Locate and identify every blood parasite.
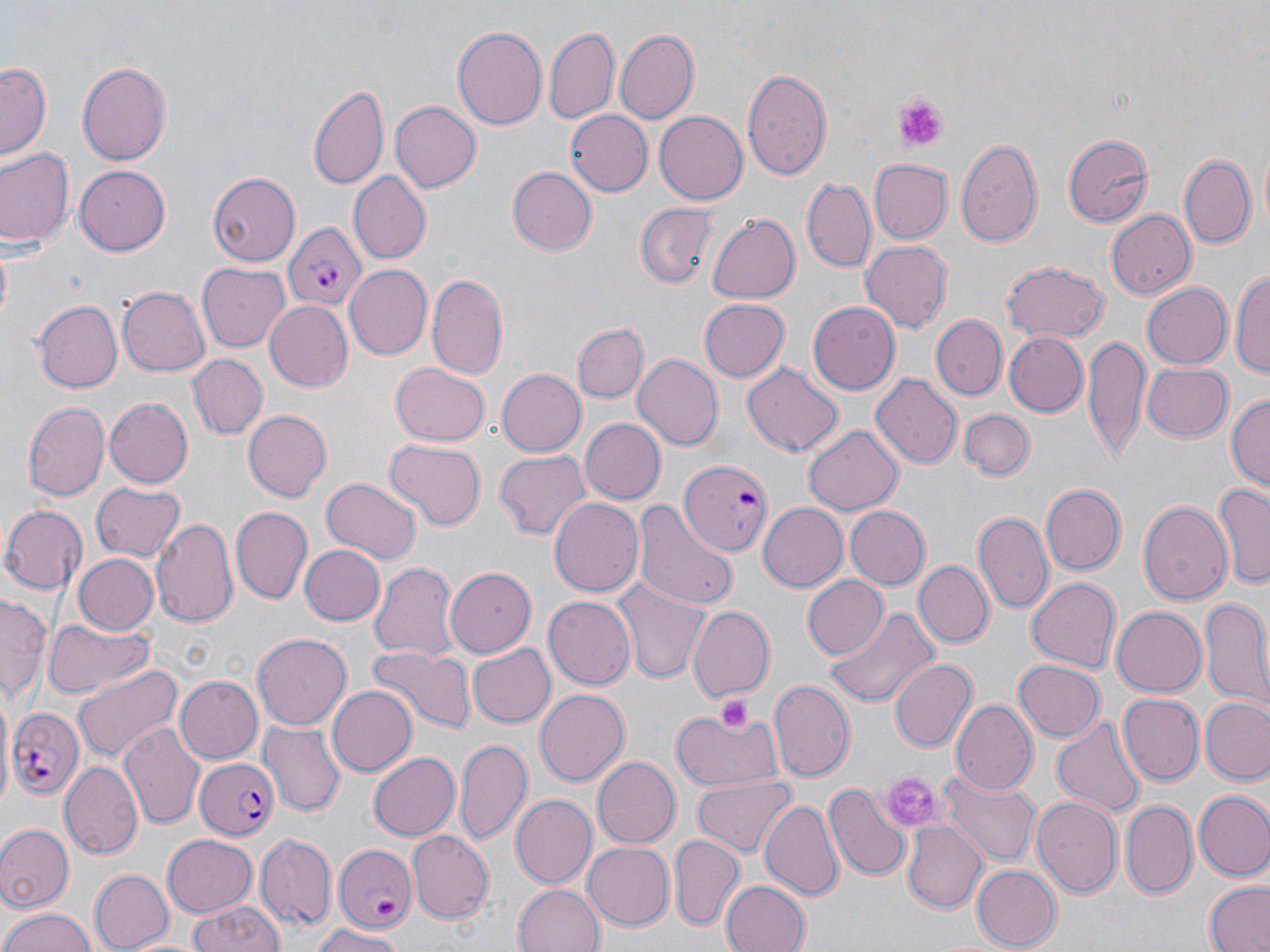
Approximate bounding boxes as (x1, y1, x2, y2) in pixels.
Plasmodium falciparum-infected red blood cells: (281, 220, 368, 311), (675, 456, 772, 559), (4, 707, 84, 799), (194, 758, 278, 841), (331, 843, 417, 934).
No Plasmodium ovale, Plasmodium malariae, Plasmodium vivax, Babesia divergens, or Trypanosoma brucei observed.

Uninfected red blood cell locations: (452, 23, 548, 132), (545, 25, 619, 125), (615, 29, 699, 125), (0, 60, 52, 160), (76, 60, 173, 166), (741, 68, 832, 183), (308, 80, 390, 190), (390, 100, 481, 193), (564, 110, 653, 197), (653, 110, 748, 205), (1064, 131, 1153, 226), (957, 138, 1042, 249), (0, 147, 77, 251), (1179, 151, 1255, 250), (868, 159, 952, 244), (73, 165, 171, 256), (507, 167, 596, 256), (207, 171, 300, 267), (347, 172, 431, 264), (803, 178, 876, 273), (637, 202, 718, 289), (1105, 209, 1194, 300), (708, 215, 800, 302), (859, 242, 952, 331), (998, 261, 1110, 342), (197, 262, 291, 353), (343, 264, 432, 362), (1233, 267, 1270, 382), (427, 273, 510, 383), (1140, 282, 1230, 370), (117, 286, 211, 378), (263, 298, 353, 390), (696, 298, 788, 383), (34, 301, 123, 392), (805, 301, 900, 395), (932, 315, 1007, 399), (572, 322, 647, 401), (1001, 331, 1087, 418), (1082, 336, 1148, 464), (188, 353, 267, 438), (631, 354, 722, 452), (739, 361, 843, 459), (1140, 362, 1231, 441), (389, 363, 489, 446), (496, 367, 586, 458), (871, 374, 961, 470), (1227, 394, 1270, 493), (104, 398, 193, 489), (23, 401, 110, 500), (960, 409, 1033, 482), (245, 410, 334, 501), (580, 419, 665, 503), (802, 425, 902, 516), (385, 439, 486, 530), (493, 451, 591, 539), (323, 479, 420, 565), (90, 482, 185, 562), (1214, 482, 1270, 587), (1042, 484, 1125, 575), (1138, 496, 1232, 608), (548, 498, 643, 598), (634, 502, 740, 611), (756, 502, 849, 591), (0, 504, 88, 591), (842, 505, 929, 590), (230, 507, 312, 604), (973, 509, 1053, 614), (151, 517, 239, 626), (299, 544, 384, 623), (74, 553, 160, 635), (369, 560, 457, 661), (915, 562, 992, 648), (445, 567, 535, 656), (802, 575, 889, 660), (613, 576, 709, 685), (1024, 576, 1121, 674), (0, 593, 48, 705), (545, 594, 638, 688), (1199, 600, 1270, 713), (827, 605, 937, 712), (688, 607, 775, 699), (1112, 608, 1206, 696), (42, 616, 155, 698), (252, 633, 352, 729), (366, 645, 472, 733), (470, 645, 555, 728), (889, 659, 976, 754), (1014, 661, 1104, 741), (72, 663, 183, 763), (175, 677, 262, 765), (769, 679, 855, 781), (327, 685, 416, 776), (534, 690, 628, 788), (1120, 693, 1206, 784), (1200, 697, 1270, 784), (949, 699, 1036, 795), (674, 708, 783, 792), (1052, 715, 1145, 819), (121, 720, 206, 830), (260, 722, 345, 817), (454, 735, 531, 846), (367, 751, 462, 841), (594, 757, 683, 848), (61, 761, 143, 858), (936, 770, 1042, 867), (691, 774, 796, 858), (824, 782, 910, 882), (1193, 790, 1270, 881), (510, 796, 595, 887), (1030, 796, 1123, 898), (760, 800, 844, 904), (1123, 802, 1197, 898), (900, 820, 989, 915), (0, 823, 72, 911), (407, 831, 494, 922), (162, 835, 259, 916), (255, 835, 335, 931), (669, 837, 744, 931), (582, 840, 672, 928), (972, 866, 1061, 948), (89, 869, 172, 951), (720, 880, 811, 952), (1203, 880, 1270, 952), (512, 882, 606, 952), (187, 898, 288, 952), (0, 906, 97, 952), (310, 925, 410, 951). Platelet locations: (893, 92, 949, 154), (715, 693, 754, 733), (882, 774, 941, 830). Slide-level diagnosis: Plasmodium falciparum. Optical microscopy. May-Grünwald-Giemsa-stained preparation. Single field of view. Image is 1270×952 pixels. Thin blood smear. 1000x magnification.